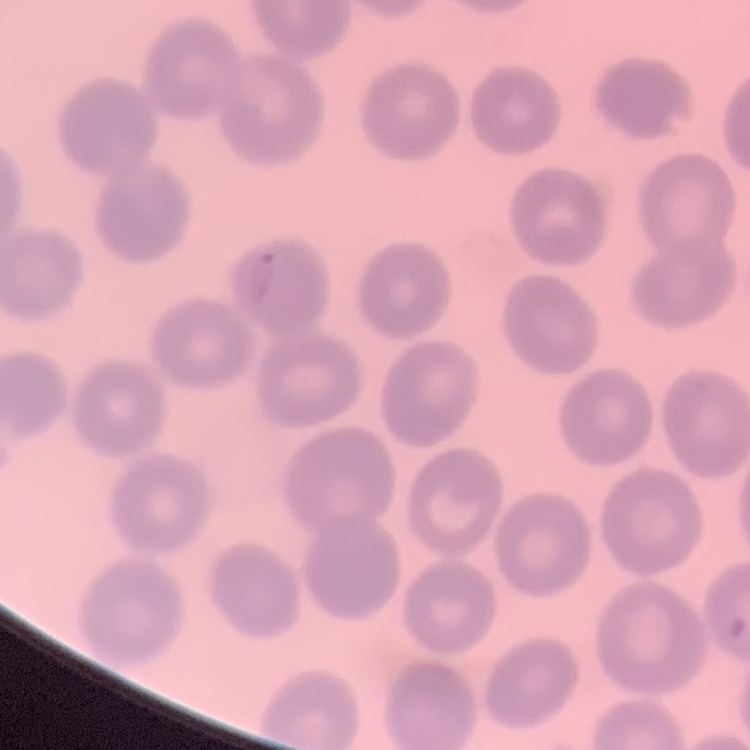
red blood cell morphology = no rouleaux formation
preparation = thin peripheral smear
stain = Field's or Giemsa
image type = one tile cut from a larger photomicrograph